Give the position of every leukocyte visible.
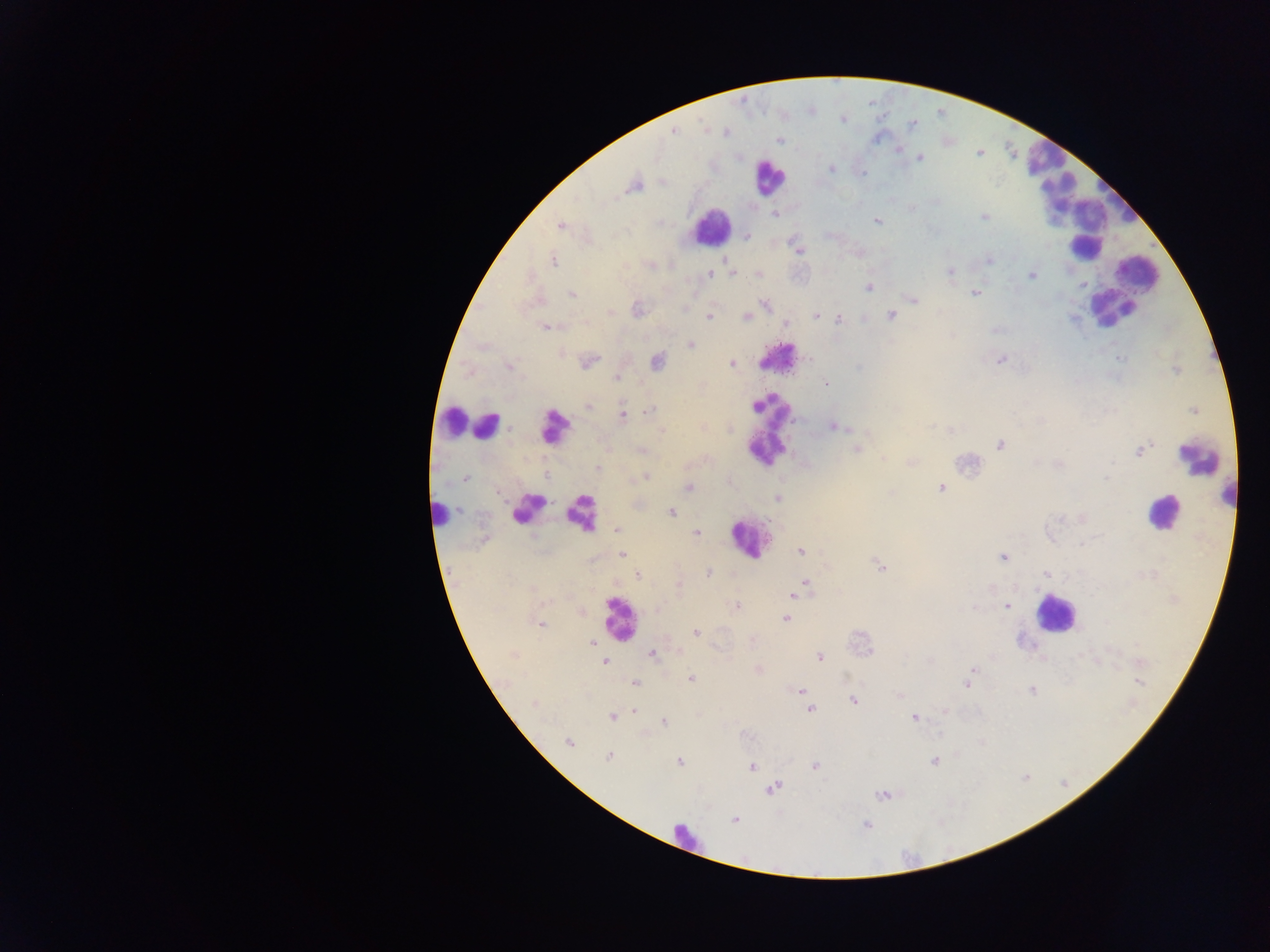
Approximate centers as x y in pixels.
Leukocytes: 1048 166; 769 176; 1085 218; 710 226; 1083 231; 1086 247; 1110 305; 779 357; 446 419; 485 426; 555 426; 767 429; 1198 457; 1230 494; 526 508; 1161 512; 578 513; 437 515; 748 538; 1054 613; 617 618; 682 840.

{
  "preparation": "thick blood smear",
  "image_size": "1270×952 pixels",
  "country": "Ghana",
  "capture": "mobile-phone photograph through a microscope",
  "field_of_view": "single",
  "malaria_parasite_locations": "approximate centers as x y in pixels: 674 131; 726 132; 778 140; 898 150; 919 158; 832 169; 863 174; 633 185; 775 214; 983 216; 877 221; 560 225; 746 236; 796 248; 988 260; 552 261; 950 271; 732 273; 708 274; 759 274; 1032 275; 868 286; 975 292; 572 294; 913 300; 765 304; 637 309; 684 309; 610 312; 815 316; 891 316; 708 317; 746 318; 838 318; 785 323; 545 326; 690 345; 1120 358; 809 359; 999 360; 589 361; 656 361; 732 364; 509 366; 858 368; 617 377; 826 383; 588 405; 649 411; 1193 411; 623 415; 835 427; 931 427; 662 430; 950 430; 1000 446; 857 450; 1140 450; 641 451; 883 459; 1059 464; 598 468; 464 477; 547 477; 646 477; 1107 477; 688 487; 941 488; 891 493; 778 498; 458 511; 671 512; 1081 517; 617 529; 696 533; 801 551; 622 555; 1003 557; 879 566; 708 573; 1046 573; 637 575; 805 583; 679 585; 799 591; 794 595; 736 606; 1006 606; 973 608; 785 619; 541 624; 695 632; 591 643; 653 654; 820 657; 604 662; 758 670; 972 670; 691 679; 1140 682; 635 683; 966 683; 801 690; 1031 690; 899 695; 853 701; 534 703; 810 709; 634 711; 944 711; 612 717; 915 717; 664 722; 569 742; 609 756; 933 761; 679 762; 752 766; 815 766; 773 788; 883 795; 735 819; 867 825"
}